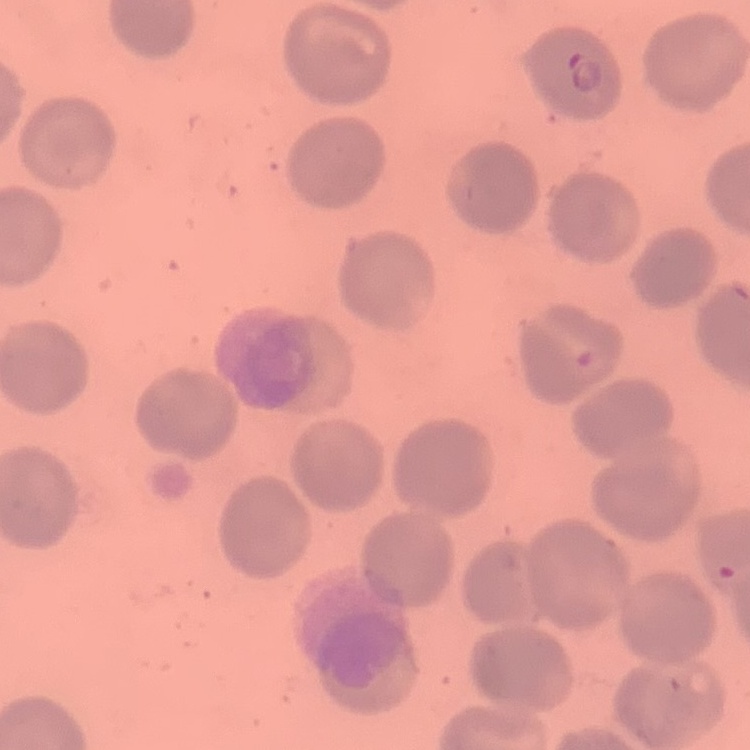
Summary:
  - Erythrocyte morphology: no rouleaux formation
  - Stain: Field's or Giemsa
  - Image type: square crop of a larger photomicrograph
  - Preparation: thin blood smear